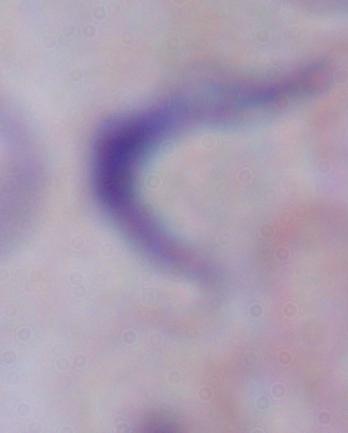

A trypanosome is seen. Photomicrograph. 1000x magnification.